Give the extent of all Plasmodium vivax-infected red blood cells.
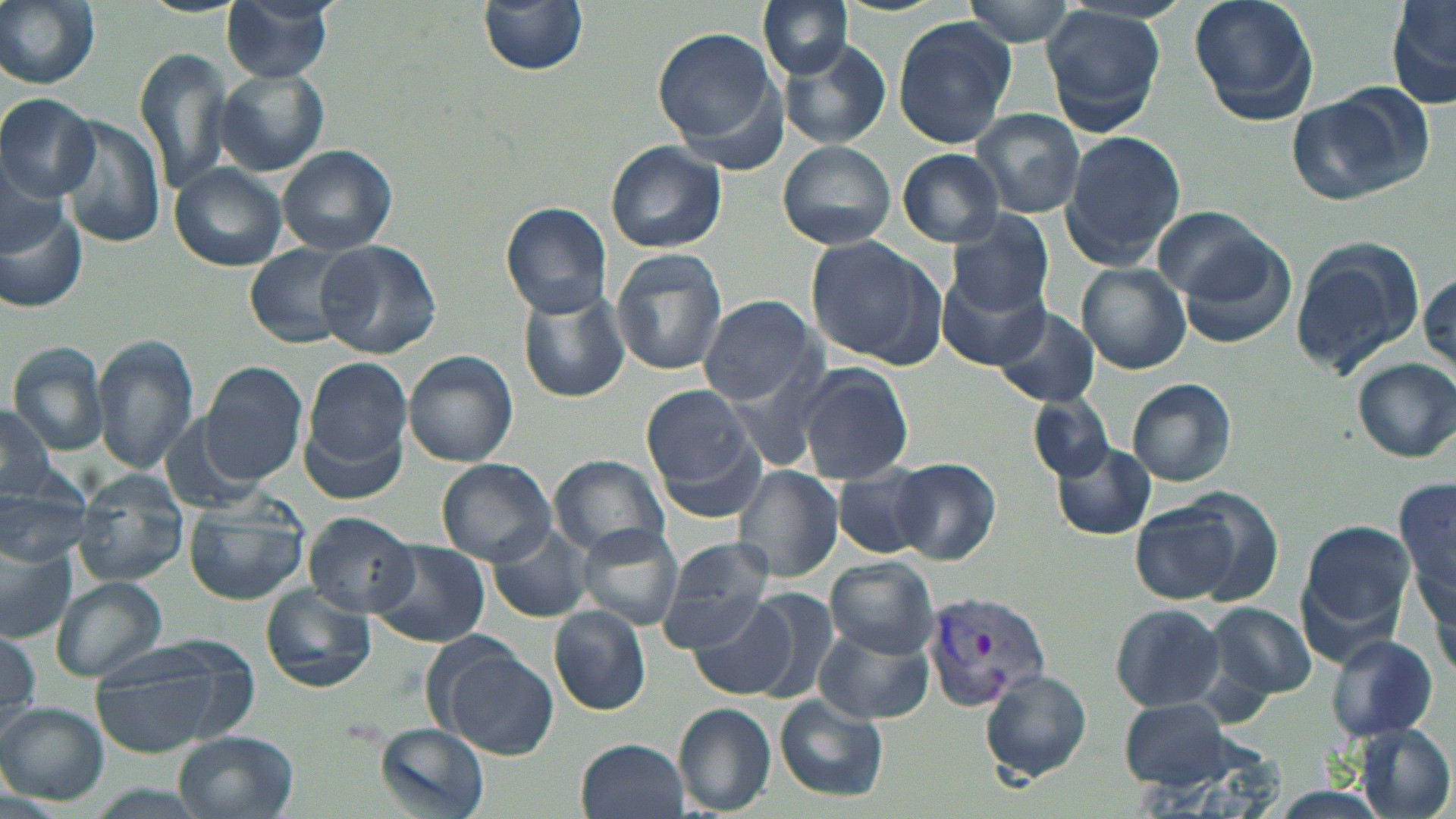

Approximate bounding boxes as [x1, y1, x2, y2] in pixels.
Plasmodium vivax-infected red blood cells: [922, 589, 1053, 713].

Summary:
  - Uninfected red blood cell locations: [0, 0, 102, 90], [221, 0, 335, 82], [479, 0, 589, 76], [758, 0, 853, 79], [962, 0, 1081, 45], [1188, 0, 1320, 126], [1386, 2, 1456, 112], [1040, 5, 1169, 136], [890, 17, 1016, 147], [653, 28, 782, 150], [779, 42, 892, 149], [135, 45, 235, 194], [216, 67, 328, 176], [1286, 87, 1427, 204], [0, 93, 98, 199], [970, 108, 1086, 219], [56, 114, 165, 249], [1058, 131, 1187, 269], [776, 140, 899, 251], [604, 141, 727, 255], [278, 146, 395, 256], [896, 149, 1006, 247], [0, 150, 69, 257], [168, 163, 287, 272], [500, 202, 612, 318], [1152, 205, 1274, 305], [0, 206, 88, 313], [947, 210, 1055, 317], [804, 236, 942, 363], [1176, 236, 1300, 348], [1288, 238, 1424, 380], [316, 240, 441, 359], [244, 243, 356, 350], [611, 248, 729, 377], [1408, 260, 1456, 382], [1078, 264, 1191, 373], [938, 267, 1052, 371], [516, 289, 628, 404], [696, 294, 818, 405], [993, 306, 1099, 408], [91, 334, 200, 474], [7, 343, 110, 454], [403, 351, 519, 467], [305, 357, 413, 473], [1351, 357, 1456, 463], [200, 361, 309, 484], [796, 362, 914, 485], [1126, 377, 1238, 487], [640, 385, 754, 491], [1029, 393, 1114, 480], [0, 406, 58, 504], [654, 437, 767, 532], [1052, 443, 1158, 538], [549, 454, 671, 558], [891, 457, 1001, 564], [437, 459, 556, 565], [735, 465, 844, 582], [836, 465, 935, 559], [0, 474, 91, 570], [75, 474, 188, 588], [1395, 477, 1455, 618], [183, 493, 312, 606], [1131, 500, 1254, 606], [303, 512, 421, 617], [1296, 518, 1416, 648], [577, 523, 684, 629], [486, 525, 593, 622], [366, 540, 489, 648], [656, 540, 777, 649], [0, 542, 77, 645], [826, 557, 942, 656], [49, 576, 168, 684], [260, 584, 376, 693], [729, 587, 837, 702], [689, 597, 797, 699], [1207, 601, 1317, 703], [1110, 602, 1226, 712], [548, 607, 651, 715], [813, 625, 935, 725], [0, 629, 42, 731], [1324, 634, 1438, 743], [87, 646, 239, 761], [440, 648, 557, 758], [980, 669, 1092, 783], [774, 693, 888, 803], [1120, 695, 1236, 788], [674, 702, 777, 815], [0, 703, 108, 803], [373, 724, 490, 817], [1353, 724, 1454, 818], [173, 731, 298, 819], [575, 737, 689, 819]
  - Slide-level diagnosis: Plasmodium vivax
  - Image size: 1456×819 pixels
  - Preparation: thin blood smear
  - Stain: May-Grünwald-Giemsa
  - Magnification: 1000x
  - Field of view: single
  - Modality: optical microscopy